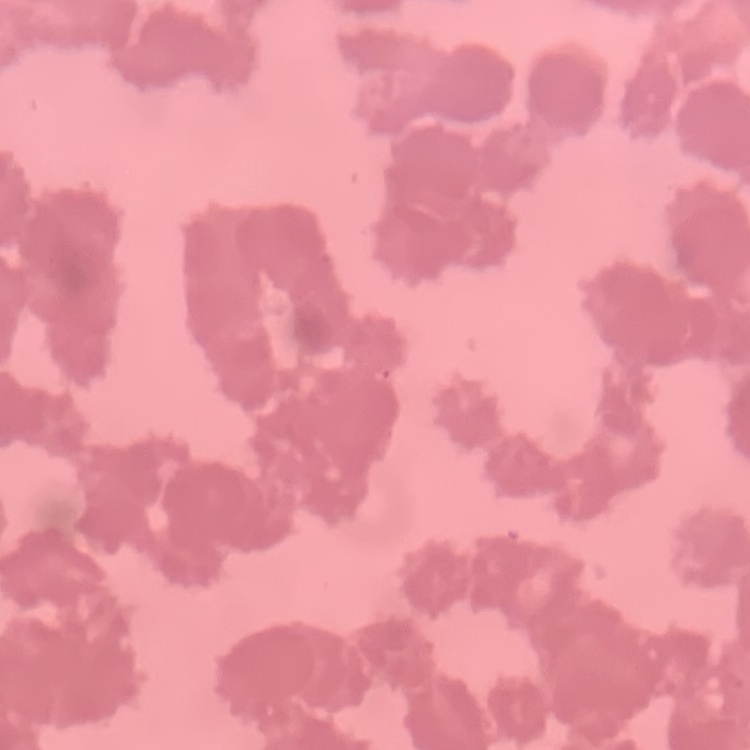 The red blood cells exhibit rouleaux formation. Thin blood film. Stained with either Field's or Giemsa. Square crop of a larger photomicrograph.